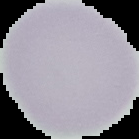

Summary:
  - Image size: 139×139 pixels
  - Malaria status: uninfected
  - Preparation: thin blood film
  - Image type: segmented cell region with the area outside set to black